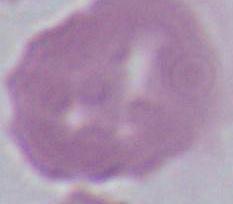 A red blood cell is seen. Micrograph. Captured at 1000x magnification.